Report the malaria status of this cell.
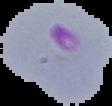
Parasitized.

From a thin blood smear. Cell region segmented out of the field of view; the surrounding area is masked to black. Image is 112×106 pixels.